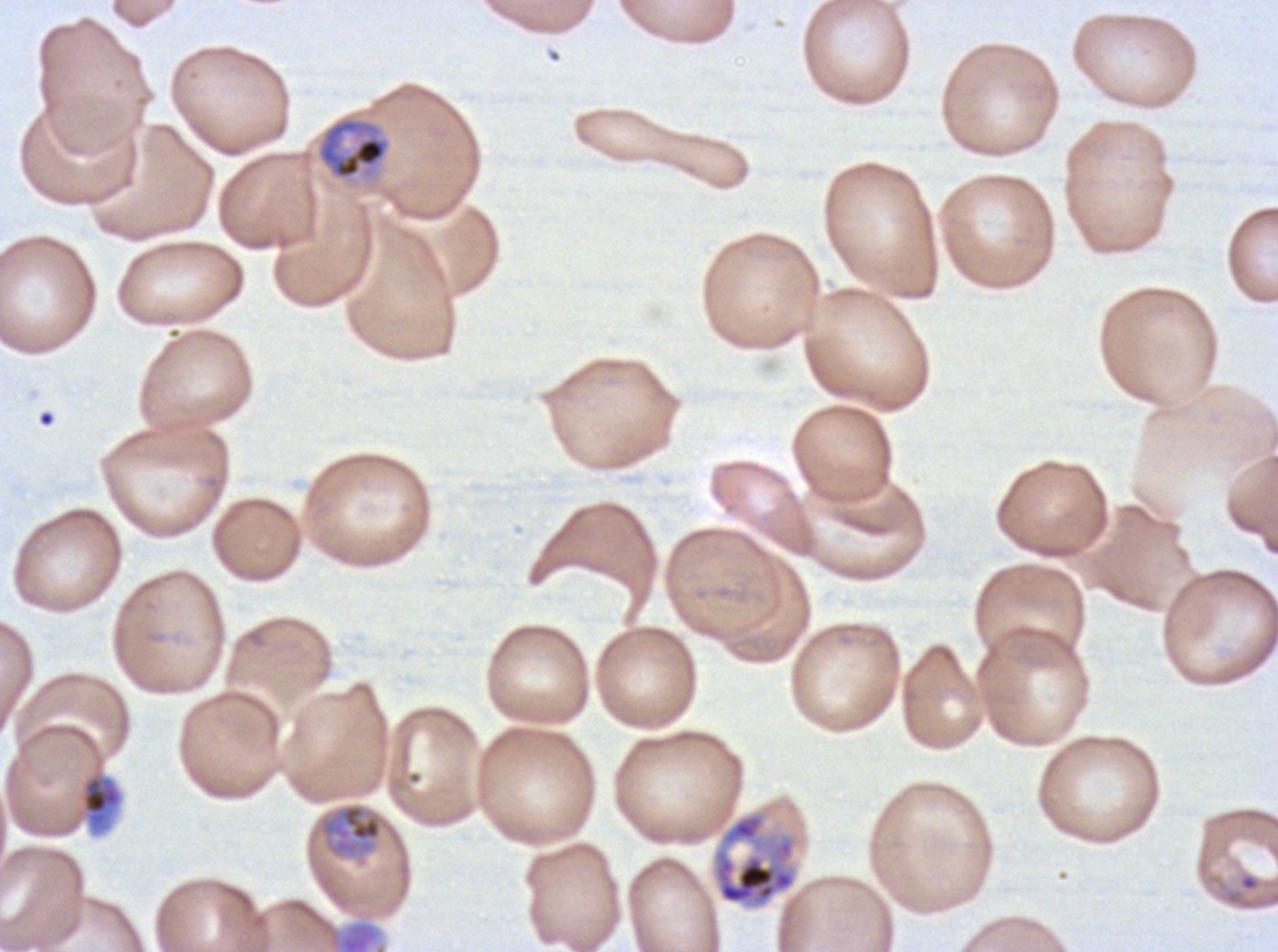
notation = approximate bounding boxes as (x1, y1, x2, y2) in pixels
late schizont locations = (711, 810, 799, 910)
mid trophozoite locations = (316, 116, 390, 180), (77, 769, 124, 836), (319, 802, 383, 859), (338, 921, 379, 951)
field of view = one sub-image of a larger composite
preparation = thin blood smear
life-cycle stages observed = mid trophozoite, late schizont
image size = 1278×952 pixels
stain = Giemsa
specimen = P. falciparum cultured ex vivo for 24 to 48 hours, from a patient in The Gambia